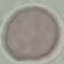

Summary:
  - Result: negative for malaria parasites
  - Preparation: thin blood film
  - Image type: cell patch, automatically extracted from a larger field of view and resized to 64 × 64 pixels
  - Capture: smartphone camera at the microscope eyepiece
  - Stain: Giemsa